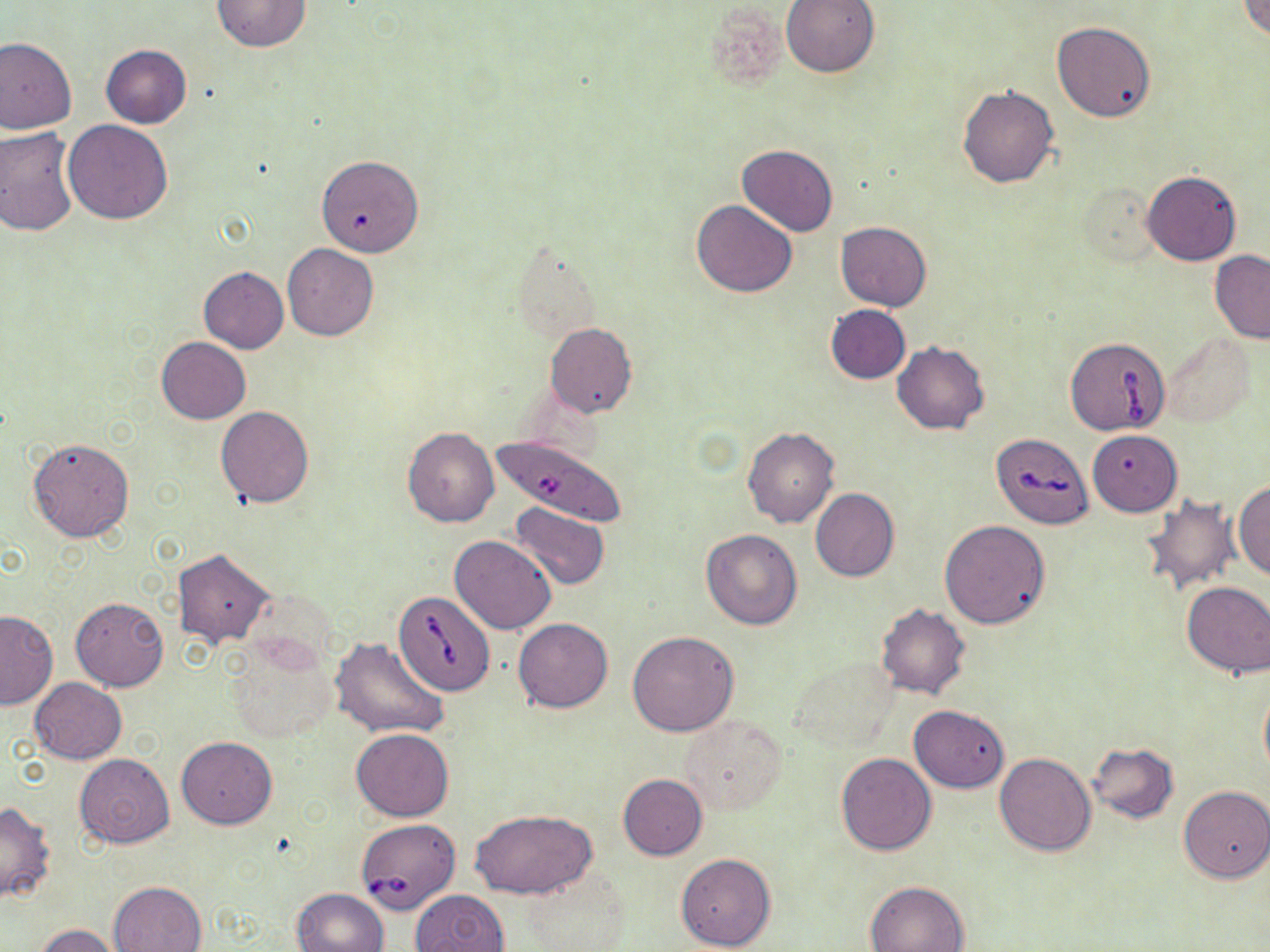

Approximate bounding boxes as (x1, y1, x2, y2) in pixels. Platelet locations: (707, 1, 792, 94). Uninfected red blood cell locations: (781, 0, 879, 77), (1237, 0, 1270, 39), (211, 1, 313, 51), (1052, 21, 1156, 122), (0, 38, 76, 133), (100, 44, 192, 128), (957, 84, 1059, 188), (63, 120, 173, 223), (0, 127, 79, 237), (738, 144, 837, 236), (315, 153, 423, 257), (1142, 171, 1242, 265), (1081, 184, 1161, 266), (691, 200, 797, 298), (835, 222, 932, 311), (283, 244, 378, 340), (1209, 250, 1270, 343), (198, 267, 289, 353), (825, 305, 911, 383), (545, 323, 637, 417), (1164, 332, 1256, 428), (156, 337, 250, 424), (892, 341, 989, 435), (215, 406, 314, 507), (402, 427, 499, 528), (742, 427, 839, 529), (1087, 429, 1182, 516), (27, 436, 134, 542), (1234, 479, 1269, 581), (811, 489, 899, 582), (1138, 494, 1241, 596), (510, 502, 610, 592), (939, 520, 1050, 629), (699, 528, 803, 629), (450, 534, 556, 634), (174, 549, 275, 648), (1181, 581, 1270, 678), (70, 596, 169, 691), (876, 603, 970, 699), (0, 609, 57, 709), (513, 618, 613, 712), (628, 631, 739, 737), (329, 636, 449, 740), (223, 637, 338, 744), (785, 657, 901, 755), (28, 677, 127, 764), (1259, 681, 1270, 781), (909, 705, 1009, 791), (680, 714, 788, 815), (351, 728, 454, 821), (176, 737, 276, 828), (1087, 742, 1178, 823), (993, 752, 1095, 856), (73, 753, 175, 848), (835, 753, 936, 855), (618, 774, 707, 860), (1178, 784, 1270, 883), (0, 801, 56, 903), (469, 810, 598, 897), (676, 853, 777, 950), (518, 866, 632, 952), (864, 880, 970, 952), (108, 881, 207, 952), (291, 888, 388, 952), (410, 889, 510, 952), (35, 923, 122, 952). Babesia divergens-infected red blood cell locations: (1065, 336, 1173, 437), (991, 432, 1094, 529), (491, 433, 630, 528), (393, 590, 495, 696), (354, 818, 461, 914). Slide-level diagnosis: Babesia divergens. 1000x magnification. Optical microscopy. Thin blood smear. May-Grünwald-Giemsa stain. One field of a larger specimen. Image is 1270×952 pixels.